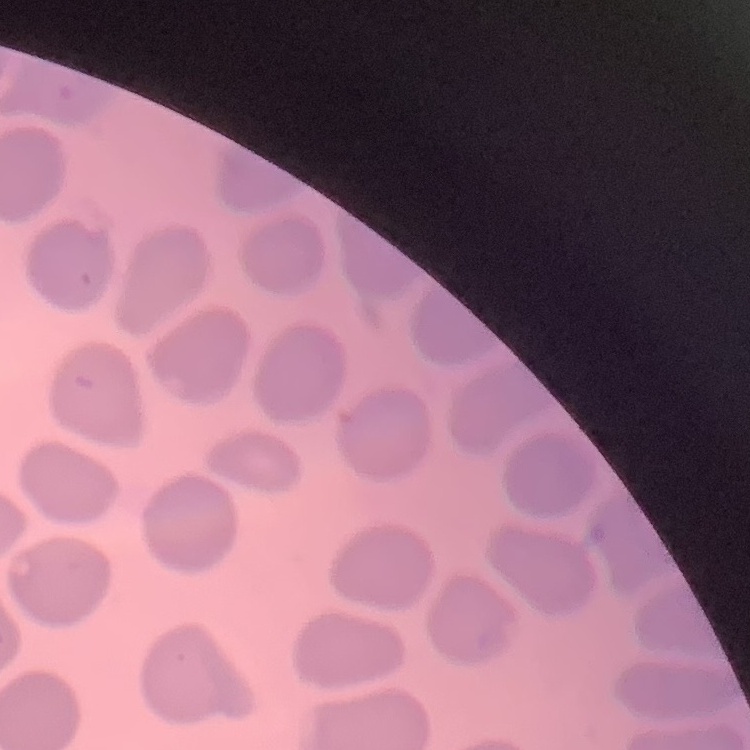

The erythrocytes exhibit no rouleaux formation. Stained with either Field's or Giemsa. Square crop of a larger photomicrograph. Thin peripheral smear.